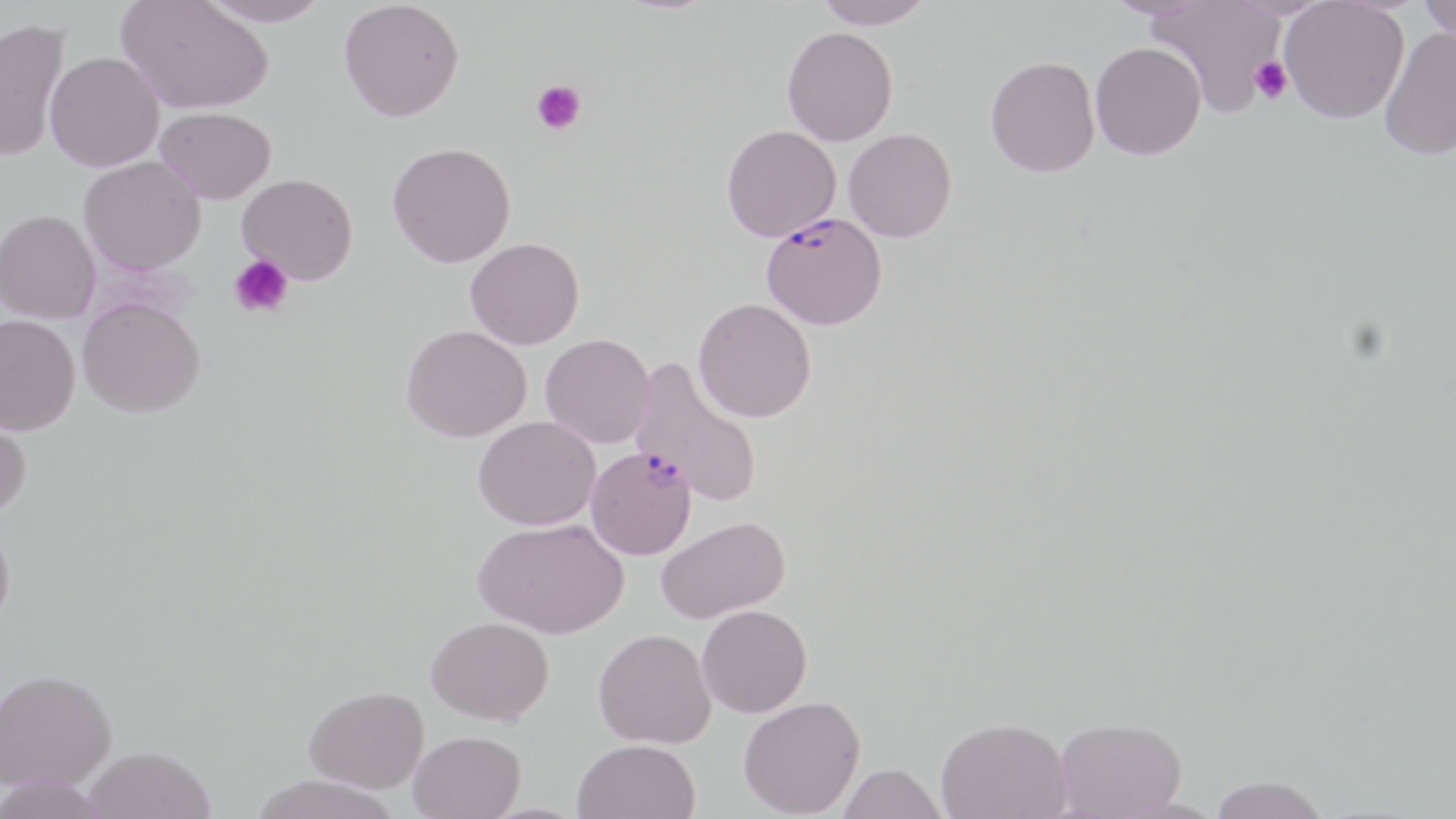

Summary:
  - Coordinate format: approximate bounding boxes as (x1,y1)-(x2,y2) corner pairs in pixels
  - Uninfected red blood cell locations: (116,0)-(273,115), (197,0)-(330,27), (339,0)-(464,122), (815,0)-(934,29), (1100,0)-(1216,20), (1418,0)-(1456,44), (1146,1)-(1285,117), (1280,1)-(1409,127), (0,17)-(71,162), (1380,26)-(1456,162), (782,27)-(898,145), (1090,42)-(1206,162), (45,51)-(164,171), (985,57)-(1100,177), (155,106)-(276,204), (721,125)-(841,242), (844,128)-(957,242), (388,142)-(515,267), (79,156)-(205,275), (237,173)-(358,284), (0,210)-(100,323), (465,237)-(584,349), (78,297)-(204,417), (693,297)-(816,422), (0,314)-(80,435), (401,324)-(531,442), (541,334)-(654,448), (631,357)-(764,509), (0,409)-(32,519), (473,416)-(600,530), (656,515)-(790,624), (473,518)-(628,637), (0,520)-(15,633), (697,605)-(812,717), (426,616)-(554,724), (594,628)-(716,748), (1,668)-(116,791), (305,685)-(429,792), (739,696)-(865,818), (936,717)-(1071,819), (1054,717)-(1187,817), (409,730)-(525,819), (572,738)-(701,819), (83,746)-(215,818), (837,763)-(948,819), (1,775)-(111,819), (246,775)-(403,819), (1205,777)-(1333,819)
  - Plasmodium falciparum-infected red blood cell locations: (756,213)-(887,331), (586,445)-(697,559)
  - Platelet locations: (1249,56)-(1292,104), (530,80)-(586,136), (229,255)-(295,318)
  - Slide-level diagnosis: Plasmodium falciparum
  - Modality: light microscopy
  - Field of view: one of a larger specimen
  - Magnification: 1000x
  - Preparation: thin blood smear
  - Stain: May-Grünwald-Giemsa
  - Image size: 1456×819 pixels